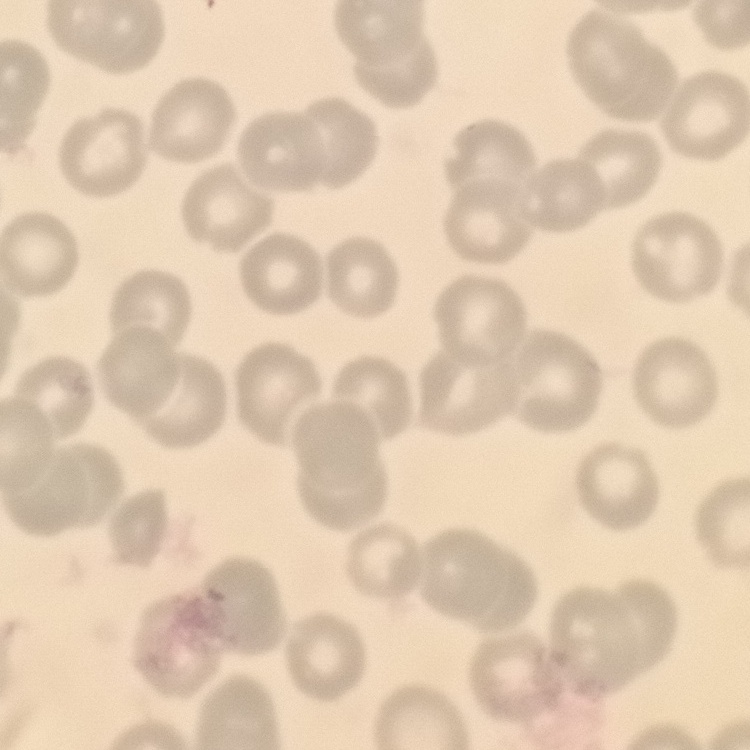
red blood cell morphology = no rouleaux formation
image type = square crop of a larger photomicrograph
stain = Field's or Giemsa
preparation = thin blood smear